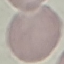
malaria status = uninfected
stain = Giemsa
image type = automatically extracted cell patch, resized to 64 × 64 pixels
capture = smartphone camera at the microscope eyepiece
preparation = thin smear